Name the blood parasite species.
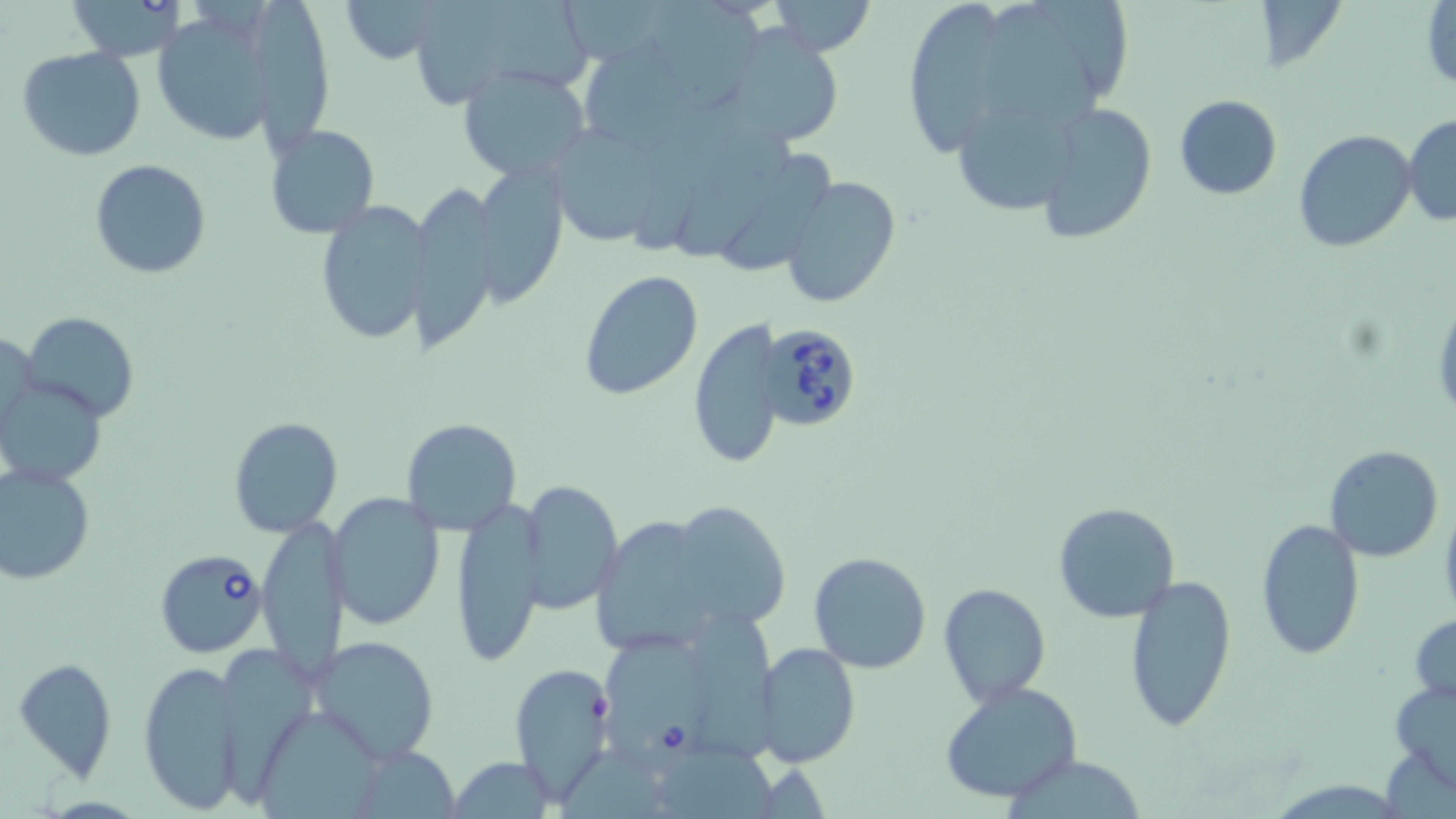
Babesia divergens.

Approximate bounding boxes as named x1/y1/x2/y2 corners in pixels. Uninfected red blood cell locations: (x1=65, y1=0, x2=188, y2=61), (x1=338, y1=0, x2=447, y2=65), (x1=653, y1=0, x2=769, y2=114), (x1=764, y1=0, x2=879, y2=55), (x1=1038, y1=0, x2=1140, y2=98), (x1=416, y1=1, x2=596, y2=102), (x1=900, y1=1, x2=1009, y2=155), (x1=987, y1=3, x2=1099, y2=129), (x1=1423, y1=3, x2=1455, y2=92), (x1=251, y1=4, x2=339, y2=161), (x1=150, y1=10, x2=279, y2=149), (x1=717, y1=26, x2=849, y2=150), (x1=571, y1=38, x2=714, y2=159), (x1=17, y1=47, x2=148, y2=163), (x1=458, y1=64, x2=594, y2=183), (x1=1173, y1=93, x2=1282, y2=201), (x1=1036, y1=102, x2=1158, y2=244), (x1=957, y1=110, x2=1080, y2=211), (x1=1403, y1=113, x2=1456, y2=227), (x1=264, y1=124, x2=380, y2=239), (x1=545, y1=125, x2=672, y2=250), (x1=678, y1=126, x2=803, y2=260), (x1=1293, y1=130, x2=1417, y2=251), (x1=732, y1=152, x2=838, y2=270), (x1=472, y1=158, x2=570, y2=309), (x1=89, y1=159, x2=211, y2=279), (x1=780, y1=174, x2=901, y2=308), (x1=410, y1=181, x2=504, y2=361), (x1=313, y1=201, x2=434, y2=346), (x1=578, y1=272, x2=703, y2=399), (x1=21, y1=312, x2=140, y2=422), (x1=689, y1=314, x2=785, y2=472), (x1=0, y1=380, x2=105, y2=484), (x1=227, y1=417, x2=342, y2=537), (x1=401, y1=418, x2=522, y2=535), (x1=1323, y1=446, x2=1444, y2=562), (x1=0, y1=462, x2=96, y2=585), (x1=519, y1=478, x2=622, y2=612), (x1=328, y1=494, x2=446, y2=632), (x1=449, y1=495, x2=548, y2=667), (x1=664, y1=498, x2=792, y2=632), (x1=1053, y1=502, x2=1180, y2=622), (x1=256, y1=517, x2=347, y2=684), (x1=1254, y1=517, x2=1367, y2=660), (x1=592, y1=519, x2=702, y2=655), (x1=806, y1=552, x2=933, y2=674), (x1=1121, y1=572, x2=1236, y2=736), (x1=937, y1=581, x2=1051, y2=706), (x1=694, y1=609, x2=786, y2=762), (x1=1410, y1=613, x2=1456, y2=705), (x1=309, y1=634, x2=442, y2=764), (x1=755, y1=642, x2=860, y2=769), (x1=221, y1=644, x2=312, y2=793), (x1=11, y1=655, x2=118, y2=776), (x1=139, y1=659, x2=246, y2=815), (x1=509, y1=660, x2=618, y2=803), (x1=1388, y1=679, x2=1456, y2=791), (x1=939, y1=681, x2=1083, y2=806), (x1=259, y1=705, x2=382, y2=819), (x1=663, y1=743, x2=782, y2=819), (x1=350, y1=746, x2=464, y2=816), (x1=1009, y1=754, x2=1145, y2=818), (x1=446, y1=758, x2=558, y2=817). Babesia divergens-infected red blood cell locations: (x1=755, y1=321, x2=865, y2=432), (x1=154, y1=549, x2=267, y2=658), (x1=604, y1=632, x2=707, y2=768). May-Grünwald-Giemsa stain. Light microscopy. Captured at 1000x magnification. Single field of view. Thin blood film. Image is 1456×819 pixels.